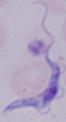

Summary:
  - Identification: trypanosome
  - Magnification: 1000x
  - Modality: micrograph